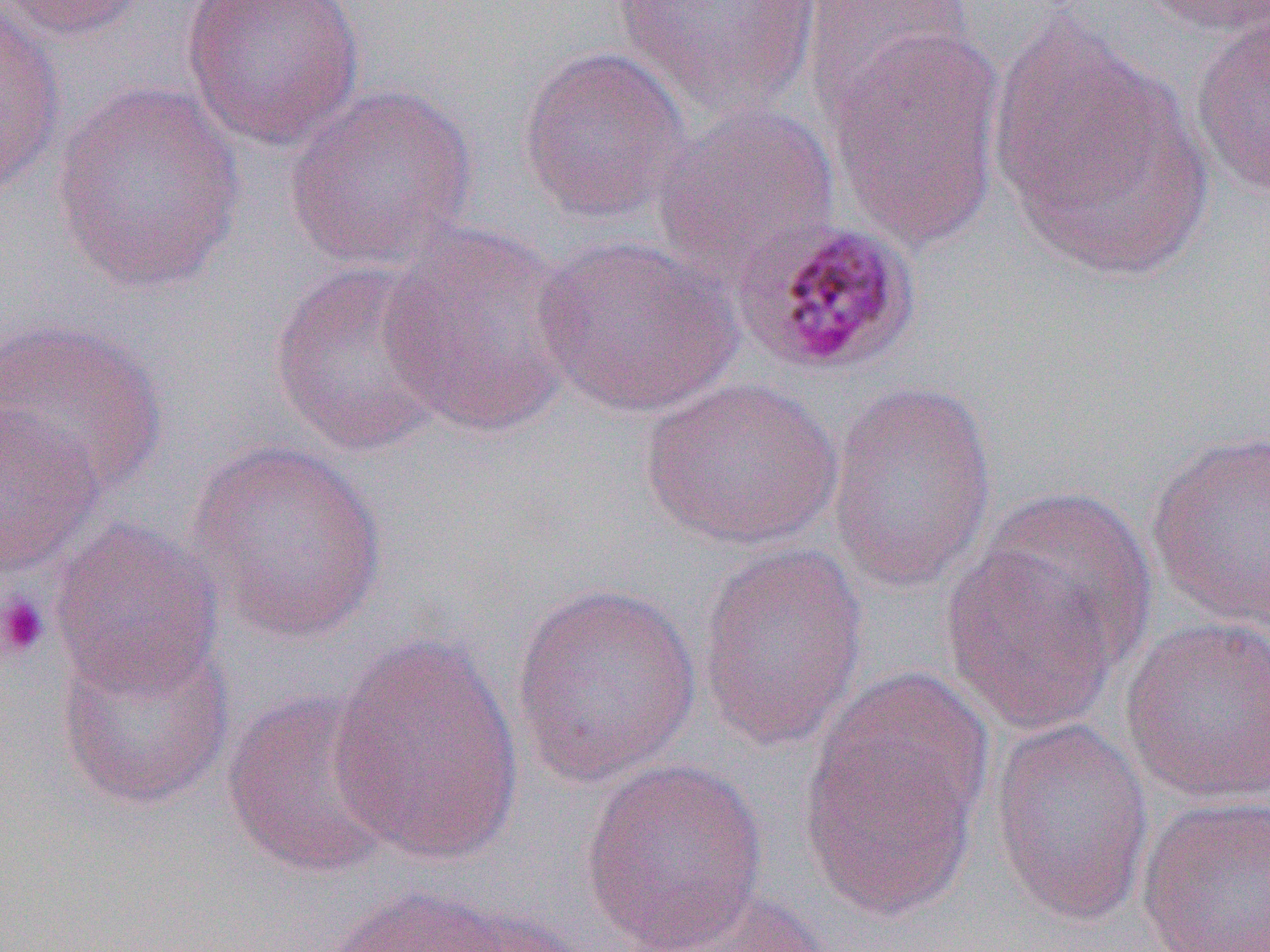

Summary:
  - Coordinate format: approximate bounding boxes as [x1, y1, x2, y2] in pixels
  - Platelet locations: [0, 592, 51, 662]
  - Plasmodium malariae-infected red blood cell locations: [733, 218, 923, 379]
  - Uninfected red blood cell locations: [0, 0, 149, 42], [0, 0, 66, 197], [181, 0, 367, 151], [611, 0, 824, 119], [1137, 0, 1270, 38], [801, 1, 976, 123], [1188, 9, 1269, 198], [987, 10, 1214, 283], [825, 27, 1007, 253], [516, 45, 690, 225], [283, 81, 479, 272], [50, 82, 246, 293], [651, 100, 841, 283], [376, 223, 584, 437], [532, 234, 746, 419], [268, 260, 453, 459], [0, 317, 170, 497], [639, 376, 843, 551], [825, 380, 999, 594], [0, 404, 105, 578], [1144, 427, 1270, 634], [187, 440, 390, 646], [49, 518, 223, 701], [941, 518, 1139, 740], [695, 542, 870, 754], [509, 580, 705, 789], [1120, 616, 1270, 806], [325, 632, 525, 865], [55, 633, 236, 812], [801, 674, 989, 919], [221, 687, 400, 880], [989, 718, 1155, 927], [579, 758, 769, 950], [1135, 794, 1270, 952], [310, 883, 552, 952], [627, 885, 831, 952]
  - Slide-level diagnosis: Plasmodium malariae
  - Field of view: one of a larger specimen
  - Preparation: thin blood film
  - Magnification: 1000x
  - Image size: 1270×952 pixels
  - Modality: light microscopy